Identify the parasite.
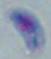

Toxoplasma gondii.

{
  "modality": "micrograph",
  "magnification": "1000x"
}